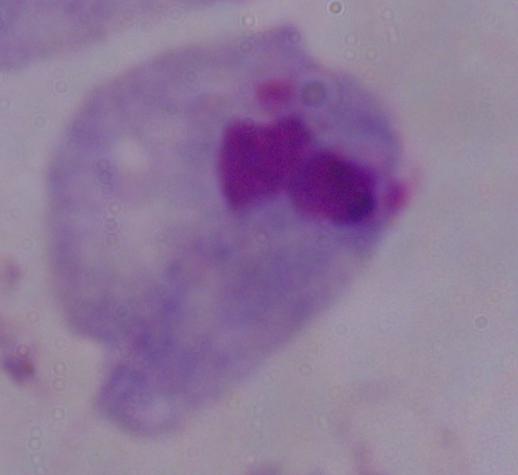

Summary:
  - Modality: micrograph
  - Magnification: 1000x
  - Identification: trichomonad